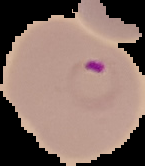
result: Plasmodium parasites identified
image_type: cell region segmented out of the field of view; surrounding area masked to black
image_size: 145×166 pixels
preparation: thin blood smear